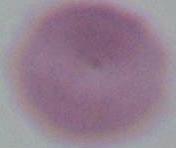

Summary:
  - Identification: red blood cell
  - Magnification: 1000x
  - Modality: micrograph